Identify the preparation type.
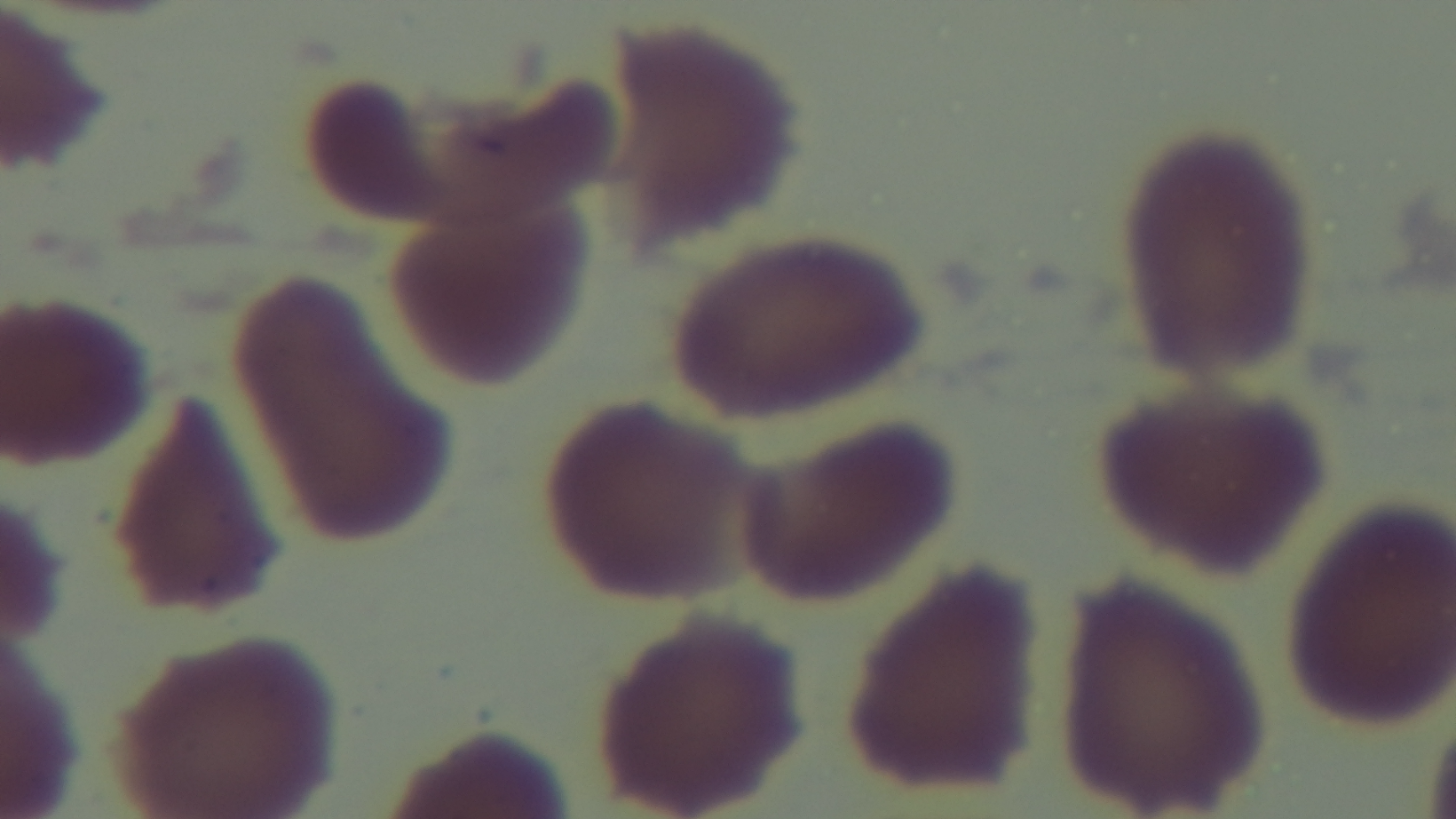

Thin.

{
  "field_of_view": "single",
  "capture": "mounted 4K digital camera",
  "objective": "100x oil immersion",
  "modality": "light microscopy",
  "malaria_status": "negative",
  "stain": "Giemsa"
}